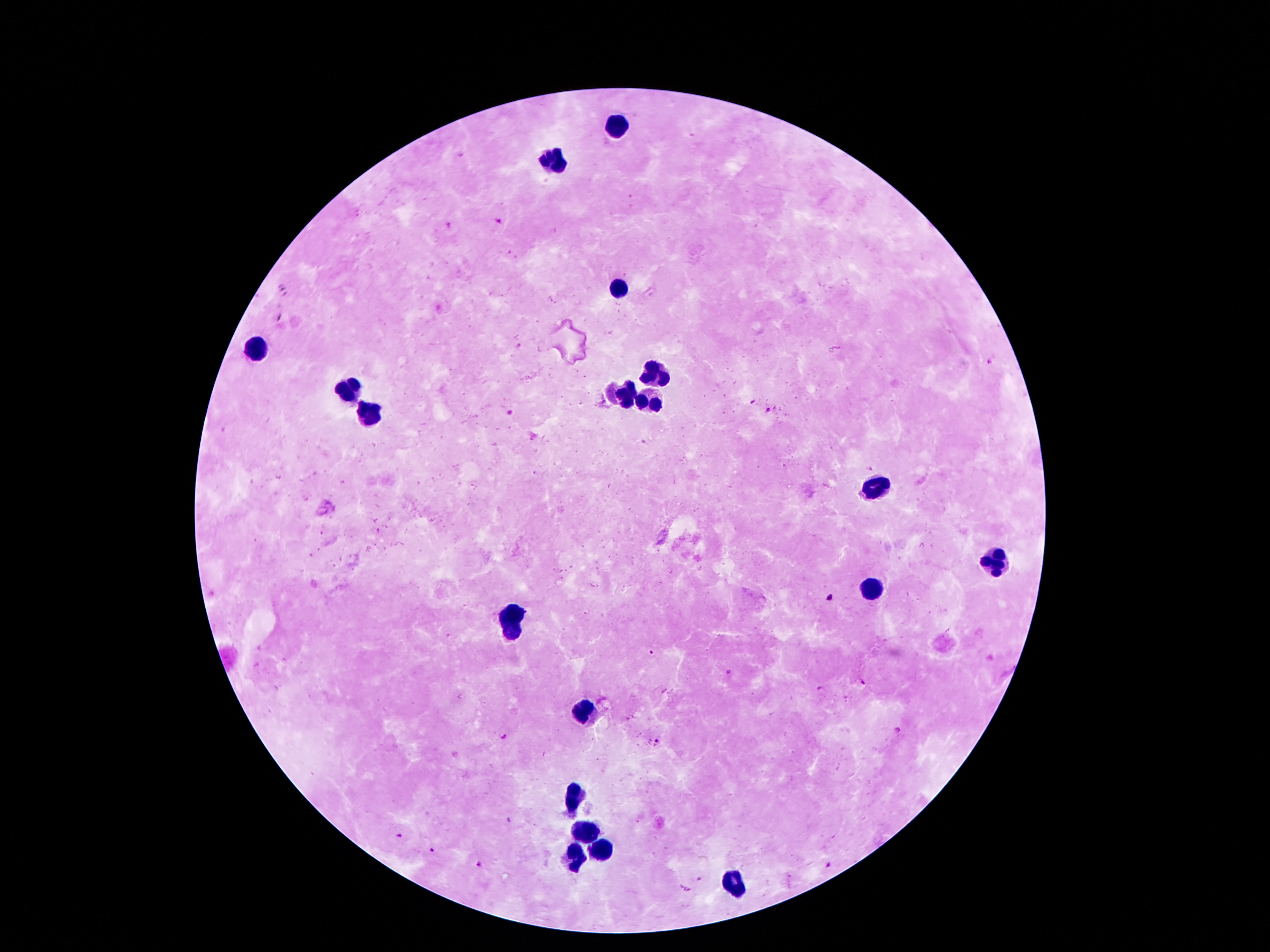
image_size: 1270×952 pixels
stain: Giemsa
magnification: 100x
preparation: thick peripheral-blood smear
leukocyte_locations: 'approximate centers as (x, y) in pixels: (615, 128), (556, 164), (622, 292), (257, 349), (658, 373), (352, 392), (625, 396), (656, 400), (368, 410), (872, 482), (990, 562), (872, 591), (515, 621), (584, 710), (577, 798), (583, 832), (597, 851), (574, 855), (733, 885)'
field_of_view: single
capture: smartphone through the microscope eyepiece
patient_malaria_status: positive for Plasmodium falciparum
plasmodium_parasite_locations: 'approximate centers as (x, y) in pixels: (462, 155), (498, 218), (447, 223), (519, 345), (989, 361), (752, 400), (770, 410), (507, 412), (644, 443), (868, 468), (380, 531), (831, 597), (448, 635), (651, 652), (728, 672), (863, 683), (821, 688), (899, 728), (503, 738), (659, 741), (509, 820), (397, 836), (432, 850), (829, 864), (477, 865), (700, 879), (687, 889)'